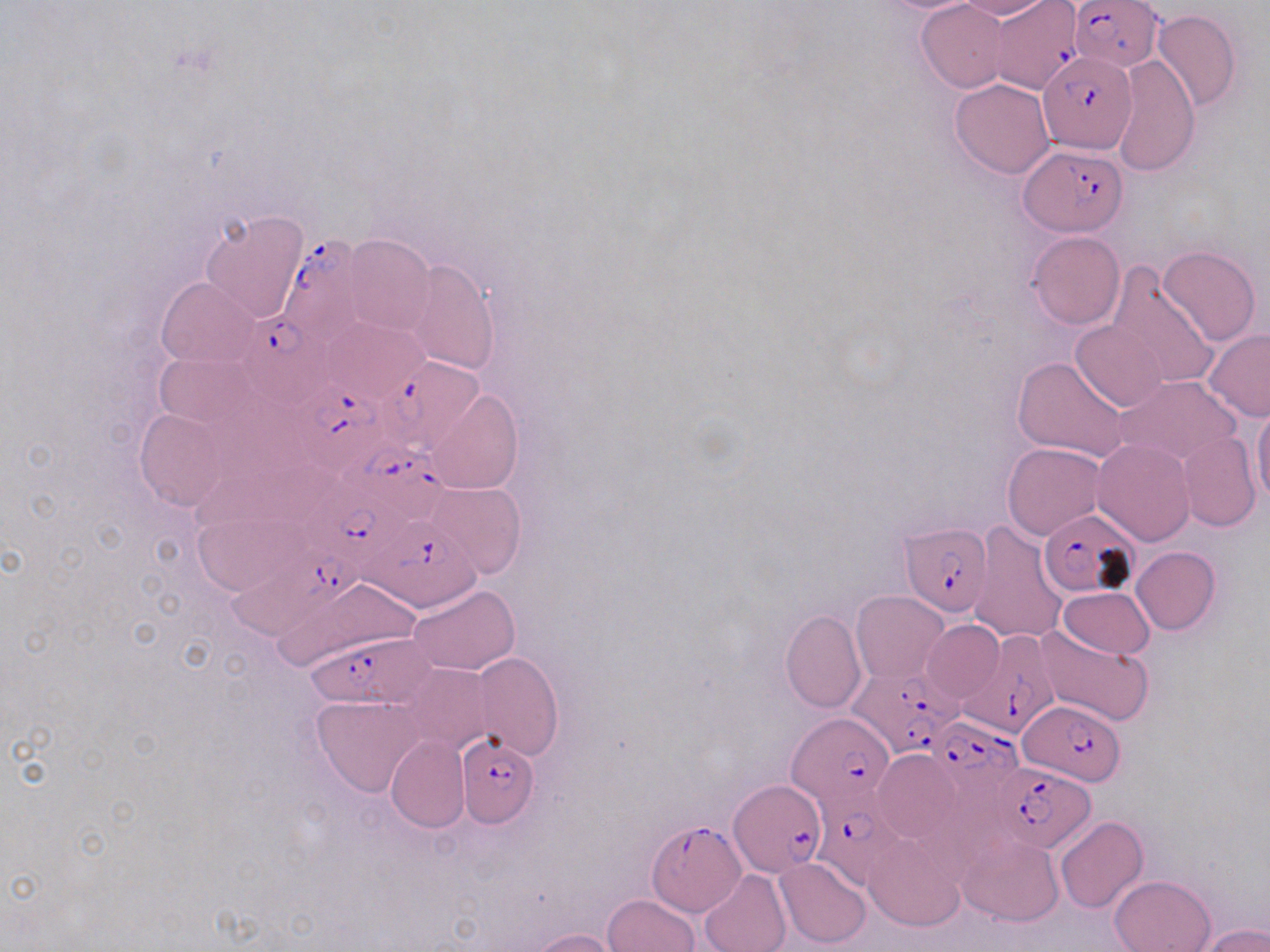

Summary:
  - Coordinate format: approximate bounding boxes as [x1, y1, x2, y2] in pixels
  - Plasmodium falciparum-infected red blood cell locations: [1070, 1, 1164, 74], [989, 2, 1081, 93], [1037, 51, 1140, 158], [1019, 144, 1129, 235], [278, 235, 370, 347], [235, 308, 339, 410], [376, 356, 485, 457], [290, 381, 401, 475], [332, 439, 451, 520], [297, 480, 422, 574], [1039, 509, 1138, 598], [369, 514, 482, 615], [900, 521, 993, 615], [216, 547, 365, 653], [960, 626, 1065, 740], [306, 633, 439, 707], [851, 667, 965, 758], [1017, 702, 1124, 783], [788, 713, 895, 810], [927, 720, 1022, 811], [456, 734, 537, 825], [992, 763, 1095, 854], [729, 777, 824, 877], [807, 796, 914, 886], [646, 823, 745, 917]
  - Uninfected red blood cell locations: [955, 0, 1053, 20], [916, 1, 1009, 93], [1152, 9, 1240, 112], [1113, 55, 1200, 175], [950, 78, 1056, 178], [201, 211, 309, 323], [1026, 231, 1124, 330], [343, 235, 435, 337], [1158, 243, 1261, 347], [406, 259, 499, 373], [1107, 265, 1220, 389], [157, 276, 260, 368], [319, 317, 426, 404], [1072, 320, 1168, 413], [1203, 330, 1270, 420], [157, 352, 259, 430], [1011, 355, 1131, 464], [1118, 375, 1236, 464], [425, 388, 523, 495], [1251, 405, 1270, 507], [132, 407, 229, 512], [1178, 432, 1260, 531], [1092, 439, 1196, 545], [1003, 442, 1104, 541], [424, 481, 527, 579], [969, 521, 1067, 644], [1132, 547, 1220, 635], [267, 575, 415, 670], [407, 584, 519, 675], [1059, 587, 1154, 658], [852, 591, 947, 682], [780, 609, 866, 713], [924, 621, 1004, 701], [1034, 626, 1154, 727], [472, 652, 563, 760], [401, 661, 493, 752], [312, 695, 424, 794], [386, 735, 469, 833], [871, 748, 961, 846], [1055, 816, 1148, 913], [862, 833, 966, 932], [956, 833, 1063, 926], [774, 857, 871, 948], [698, 869, 791, 952], [1110, 875, 1215, 952], [602, 894, 699, 952], [1200, 924, 1270, 952], [529, 928, 621, 952]
  - Slide-level diagnosis: Plasmodium falciparum
  - Modality: light microscopy
  - Stain: May-Grünwald-Giemsa
  - Preparation: thin blood film
  - Magnification: 1000x
  - Image size: 1270×952 pixels
  - Field of view: one of a larger specimen